State which parasite is depicted.
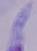
A trypanosome.

{
  "magnification": "1000x",
  "modality": "micrograph"
}